Locate every blood parasite and identify its species.
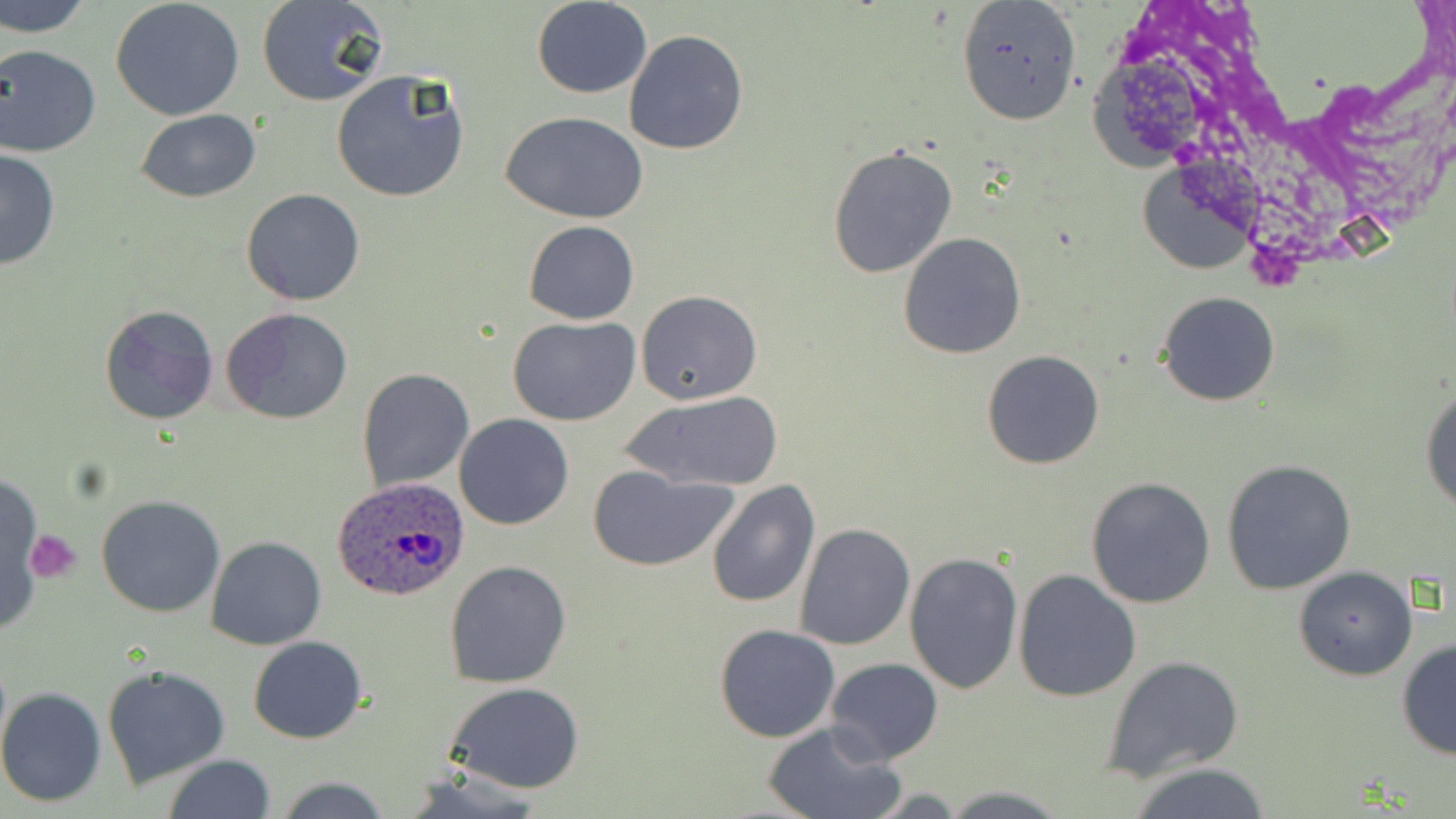
Approximate bounding boxes as named x1/y1/x2/y2 corners in pixels.
Plasmodium ovale-infected red blood cells: (x1=330, y1=476, x2=472, y2=600).
No Plasmodium falciparum, Plasmodium malariae, Plasmodium vivax, Babesia divergens, or Trypanosoma brucei observed.

slide-level diagnosis = Plasmodium ovale
image size = 1456×819 pixels
platelet locations = approximate bounding boxes as named x1/y1/x2/y2 corners in pixels: (x1=27, y1=528, x2=80, y2=583)
uninfected red blood cell locations = approximate bounding boxes as named x1/y1/x2/y2 corners in pixels: (x1=2, y1=0, x2=94, y2=38), (x1=110, y1=0, x2=245, y2=119), (x1=255, y1=0, x2=388, y2=107), (x1=955, y1=0, x2=1083, y2=126), (x1=531, y1=1, x2=653, y2=98), (x1=623, y1=29, x2=748, y2=156), (x1=0, y1=45, x2=102, y2=158), (x1=331, y1=70, x2=470, y2=203), (x1=136, y1=108, x2=261, y2=201), (x1=499, y1=110, x2=652, y2=223), (x1=827, y1=144, x2=957, y2=278), (x1=0, y1=147, x2=61, y2=272), (x1=241, y1=189, x2=366, y2=307), (x1=523, y1=220, x2=638, y2=324), (x1=898, y1=233, x2=1027, y2=359), (x1=636, y1=290, x2=763, y2=406), (x1=1157, y1=291, x2=1281, y2=407), (x1=99, y1=304, x2=218, y2=426), (x1=220, y1=309, x2=352, y2=426), (x1=507, y1=316, x2=640, y2=424), (x1=980, y1=349, x2=1106, y2=470), (x1=356, y1=367, x2=474, y2=493), (x1=1420, y1=379, x2=1456, y2=518), (x1=619, y1=390, x2=785, y2=493), (x1=454, y1=413, x2=574, y2=531), (x1=1223, y1=459, x2=1356, y2=595), (x1=587, y1=465, x2=740, y2=571), (x1=0, y1=472, x2=42, y2=632), (x1=1086, y1=476, x2=1217, y2=609), (x1=705, y1=479, x2=819, y2=609), (x1=96, y1=494, x2=225, y2=618), (x1=794, y1=523, x2=916, y2=650), (x1=205, y1=535, x2=327, y2=650), (x1=904, y1=552, x2=1024, y2=694), (x1=443, y1=559, x2=572, y2=688), (x1=1292, y1=564, x2=1418, y2=680), (x1=1013, y1=568, x2=1142, y2=702), (x1=714, y1=624, x2=840, y2=742), (x1=248, y1=635, x2=368, y2=743), (x1=1395, y1=638, x2=1456, y2=760), (x1=1103, y1=654, x2=1246, y2=781), (x1=825, y1=657, x2=943, y2=764), (x1=102, y1=663, x2=231, y2=791), (x1=444, y1=681, x2=587, y2=794), (x1=0, y1=688, x2=107, y2=807), (x1=759, y1=719, x2=905, y2=819), (x1=161, y1=755, x2=277, y2=819), (x1=1126, y1=764, x2=1274, y2=818), (x1=398, y1=769, x2=548, y2=817), (x1=274, y1=776, x2=393, y2=818), (x1=938, y1=786, x2=1074, y2=817)
field of view = single
preparation = thin blood smear
stain = May-Grünwald-Giemsa
modality = light microscopy
magnification = 1000x